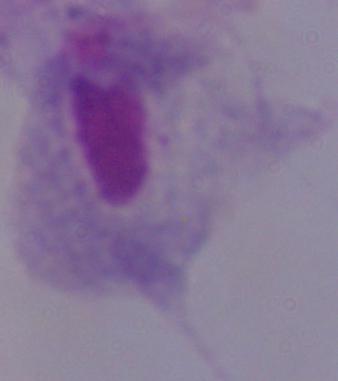
{
  "identification": "trichomonad",
  "magnification": "1000x",
  "modality": "micrograph"
}